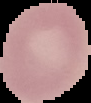

{
  "image_size": "91×103 pixels",
  "result": "no malaria parasites detected",
  "preparation": "thin blood smear",
  "image_type": "segmented cell region on a black background"
}